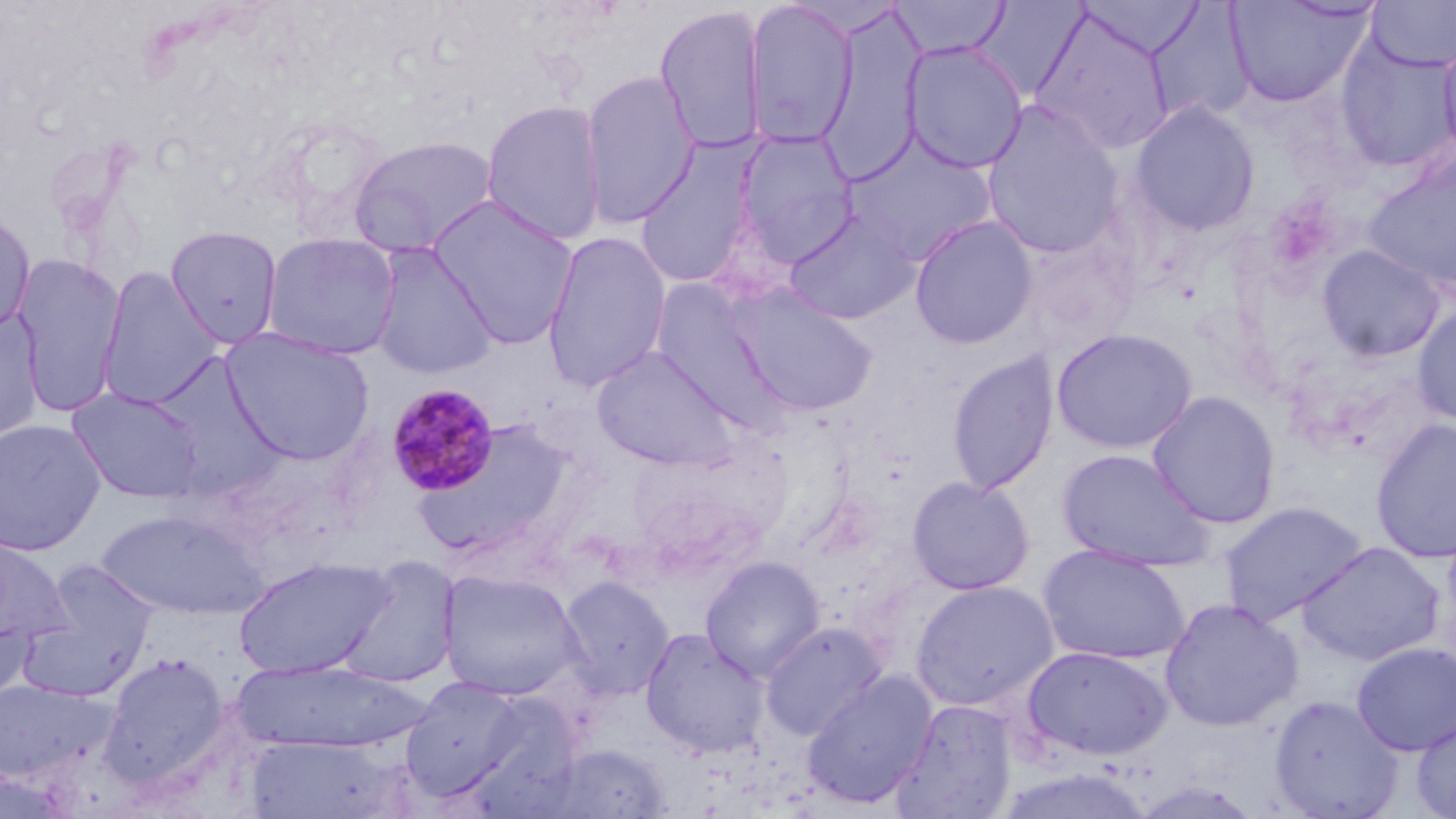

Approximate bounding boxes as (x1, y1, x2, y2) in pixels. Plasmodium malariae-infected red blood cell locations: (386, 383, 501, 498). Uninfected red blood cell locations: (889, 0, 1010, 59), (1078, 0, 1205, 60), (1365, 0, 1456, 73), (743, 1, 858, 149), (1225, 1, 1373, 106), (970, 2, 1089, 101), (653, 4, 768, 155), (1147, 4, 1255, 126), (816, 7, 927, 185), (1029, 8, 1176, 153), (1437, 32, 1456, 165), (1336, 37, 1456, 173), (901, 40, 1028, 174), (579, 69, 700, 229), (481, 99, 607, 246), (1129, 100, 1260, 236), (981, 101, 1124, 259), (733, 129, 859, 265), (347, 133, 500, 257), (843, 137, 998, 265), (635, 145, 760, 289), (1362, 150, 1456, 297), (429, 196, 579, 349), (0, 207, 36, 335), (784, 210, 920, 325), (910, 214, 1038, 349), (165, 225, 282, 348), (542, 231, 672, 393), (262, 232, 402, 360), (1018, 232, 1141, 351), (368, 243, 497, 380), (1316, 244, 1447, 362), (13, 253, 126, 416), (96, 267, 223, 410), (651, 283, 782, 424), (727, 285, 879, 417), (1411, 301, 1456, 429), (0, 307, 45, 444), (221, 327, 376, 466), (1051, 328, 1198, 453), (592, 346, 738, 471), (946, 350, 1060, 496), (67, 387, 206, 503), (1147, 391, 1281, 529), (0, 418, 106, 556), (410, 418, 578, 560), (1370, 419, 1456, 563), (1056, 448, 1214, 572), (907, 476, 1035, 595), (1219, 500, 1370, 626), (96, 508, 265, 619), (0, 539, 74, 648), (1297, 542, 1445, 665), (1039, 544, 1190, 665), (700, 555, 826, 682), (232, 557, 395, 679), (335, 557, 461, 688), (18, 560, 160, 701), (438, 569, 583, 701), (557, 576, 674, 700), (910, 579, 1059, 712), (1159, 598, 1303, 732), (0, 613, 36, 706), (759, 621, 886, 740), (640, 627, 770, 758), (1351, 642, 1455, 756), (1022, 645, 1173, 761), (99, 652, 231, 788), (230, 659, 430, 751), (801, 670, 938, 809), (400, 676, 527, 799), (0, 680, 116, 784), (1268, 694, 1404, 818), (891, 698, 1018, 818), (1412, 715, 1456, 818), (244, 734, 398, 818), (542, 743, 675, 817). Slide-level diagnosis: Plasmodium malariae. May-Grünwald-Giemsa-stained preparation. Image is 1456×819 pixels. Captured at 1000x magnification. One field of a larger specimen. Thin blood film. Light microscopy.